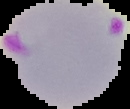

Summary:
  - Result: malaria parasites detected
  - Preparation: thin blood film
  - Image type: segmented cell region with the area outside set to black
  - Image size: 130×109 pixels